Locate and identify every blood parasite.
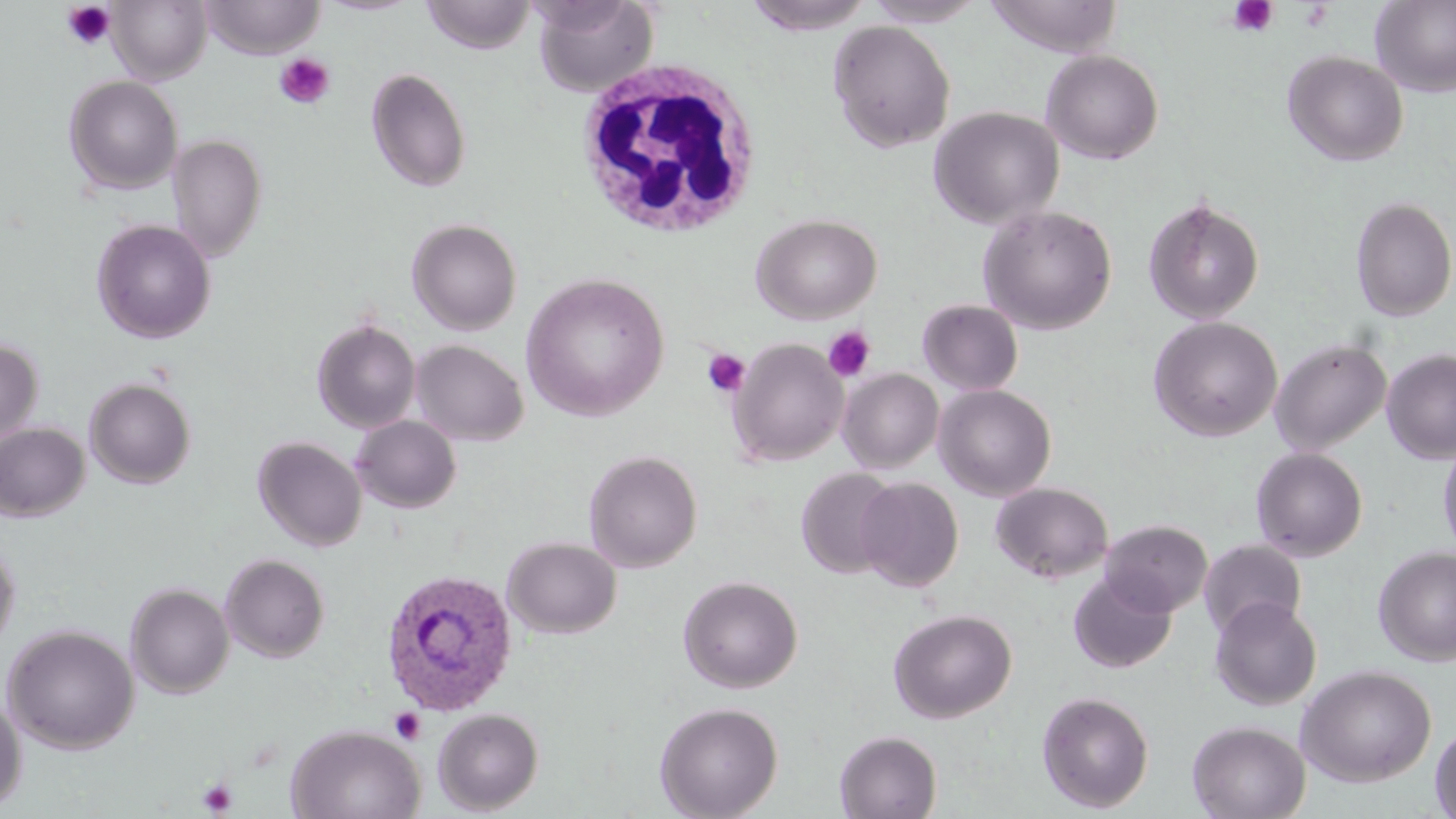
Approximate bounding boxes as (x1, y1, x2, y2) in pixels.
Plasmodium ovale-infected red blood cells: (381, 567, 518, 717).
No Plasmodium falciparum, Plasmodium malariae, Plasmodium vivax, Babesia divergens, or Trypanosoma brucei observed.

Platelet locations: (1228, 0, 1278, 37), (61, 2, 118, 51), (1298, 2, 1333, 32), (274, 53, 335, 110), (822, 326, 876, 382), (702, 348, 751, 398), (390, 708, 426, 745), (197, 777, 238, 816). Uninfected red blood cell locations: (199, 0, 326, 60), (318, 0, 420, 16), (421, 0, 536, 54), (532, 0, 659, 96), (742, 0, 877, 35), (864, 0, 989, 27), (984, 0, 1123, 58), (1370, 0, 1456, 97), (108, 1, 211, 84), (828, 20, 955, 152), (1041, 50, 1164, 164), (1282, 51, 1409, 166), (366, 67, 472, 193), (63, 75, 183, 195), (928, 106, 1064, 229), (168, 134, 267, 261), (1350, 196, 1456, 322), (1143, 197, 1265, 325), (978, 205, 1117, 335), (752, 213, 883, 323), (407, 218, 522, 335), (91, 219, 216, 343), (520, 273, 670, 421), (917, 299, 1024, 396), (1148, 316, 1283, 442), (312, 318, 421, 433), (0, 337, 43, 445), (729, 337, 848, 467), (1270, 337, 1392, 456), (411, 339, 528, 447), (1381, 348, 1456, 465), (838, 368, 944, 473), (84, 377, 197, 489), (934, 384, 1057, 501), (351, 415, 461, 513), (0, 423, 90, 522), (252, 436, 367, 552), (1437, 438, 1456, 560), (1250, 447, 1368, 561), (584, 450, 703, 572), (796, 467, 901, 578), (856, 477, 964, 592), (991, 482, 1113, 583), (1101, 520, 1212, 617), (0, 537, 20, 655), (503, 537, 621, 639), (1199, 539, 1307, 640), (1373, 545, 1456, 666), (219, 553, 330, 663), (1068, 572, 1176, 673), (678, 575, 803, 693), (125, 582, 235, 699), (1209, 596, 1321, 711), (889, 608, 1017, 723), (2, 624, 140, 754), (1296, 664, 1437, 787), (0, 691, 26, 812), (1036, 691, 1155, 812), (654, 700, 784, 818), (432, 707, 544, 814), (1187, 720, 1310, 819), (286, 723, 426, 819), (1430, 723, 1456, 819), (835, 730, 942, 819). White blood cell locations: (571, 56, 761, 240). Slide-level diagnosis: Plasmodium ovale. 1000x magnification. May-Grünwald-Giemsa stain. Optical microscopy. Thin blood film. Single field of view. Image is 1456×819 pixels.